Name the cell type shown.
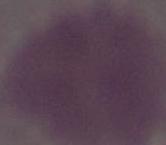
An erythrocyte.

Captured at 1000x magnification. Micrograph.